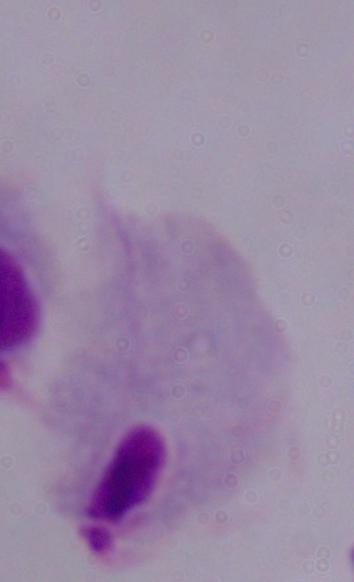
{
  "identification": "trichomonad",
  "modality": "photomicrograph",
  "magnification": "1000x"
}